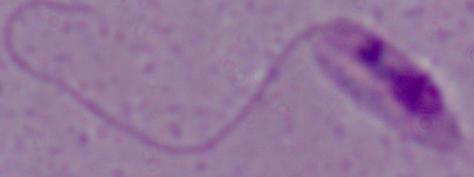
A Leishmania parasite is seen. Photomicrograph. 1000x magnification.